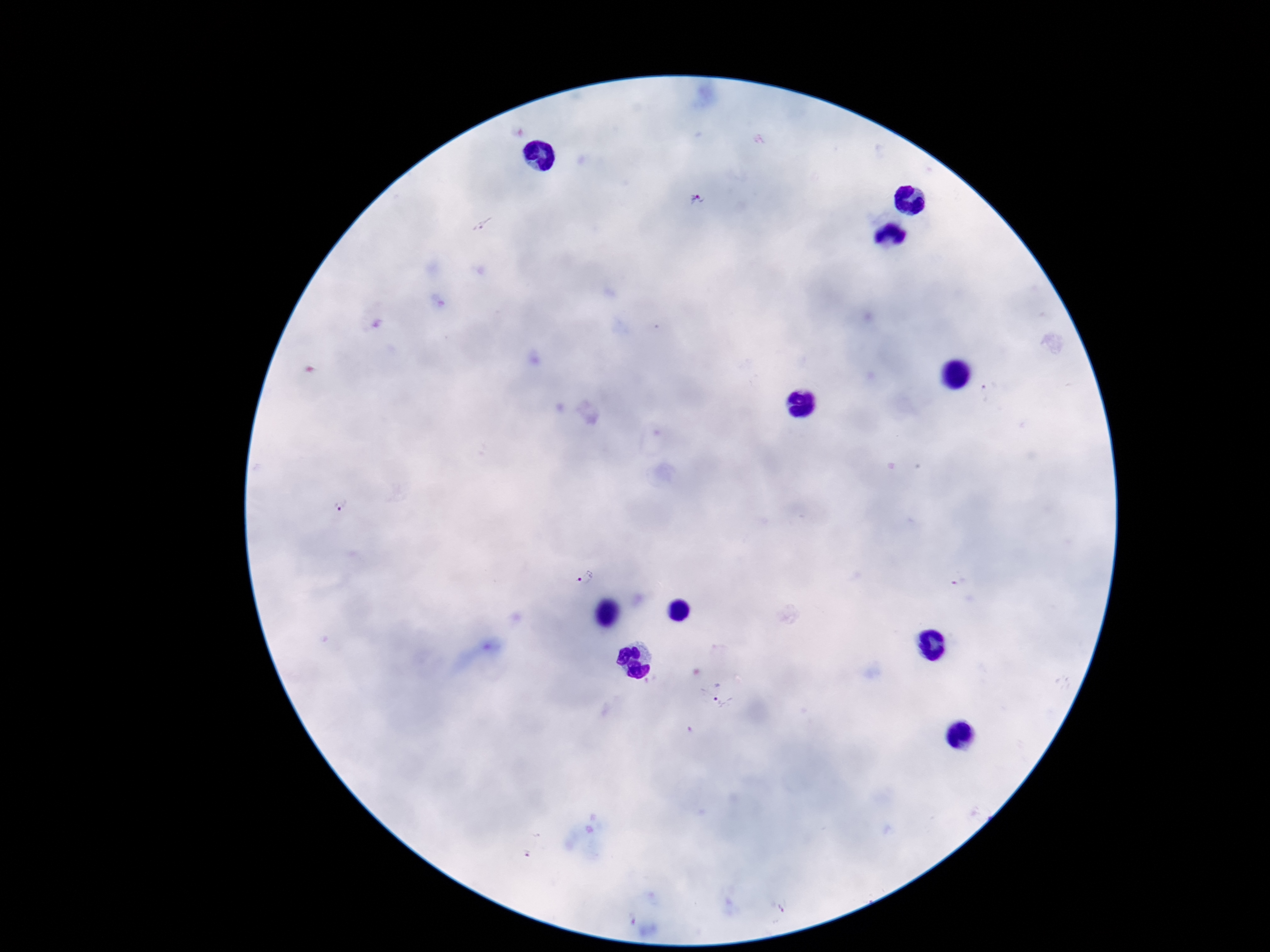

Approximate centers as (x, y) in pixels. Plasmodium parasite locations: (695, 200), (479, 225), (342, 508), (583, 575), (723, 707). One field from this slide. Photographed through the microscope eyepiece with a smartphone camera. Giemsa-stained preparation. 100x magnification. Patient malaria status: infected. Image is 1270×952 pixels. Thick blood film.